Report the malaria status of this cell.
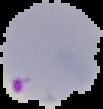

Parasitized.

Image is 103×109 pixels. From a thin blood smear. Segmented cell region on a black background.